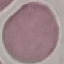

malaria status = uninfected
stain = Giemsa
image type = cell patch, automatically extracted from a larger field of view and resized to 64 × 64 pixels
preparation = thin blood film
capture = smartphone through the microscope eyepiece